Report the malaria status of this cell.
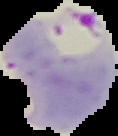
It is parasitized.

Summary:
  - Image size: 118×136 pixels
  - Image type: cell region segmented out of the field of view; surrounding area masked to black
  - Preparation: thin blood smear